Report the malaria status of this cell.
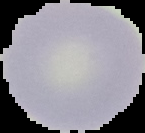
Uninfected.

image_type: cell region segmented out of the field of view; surrounding area masked to black
preparation: thin blood film
image_size: 145×133 pixels